Assess the morphology of the erythrocytes.
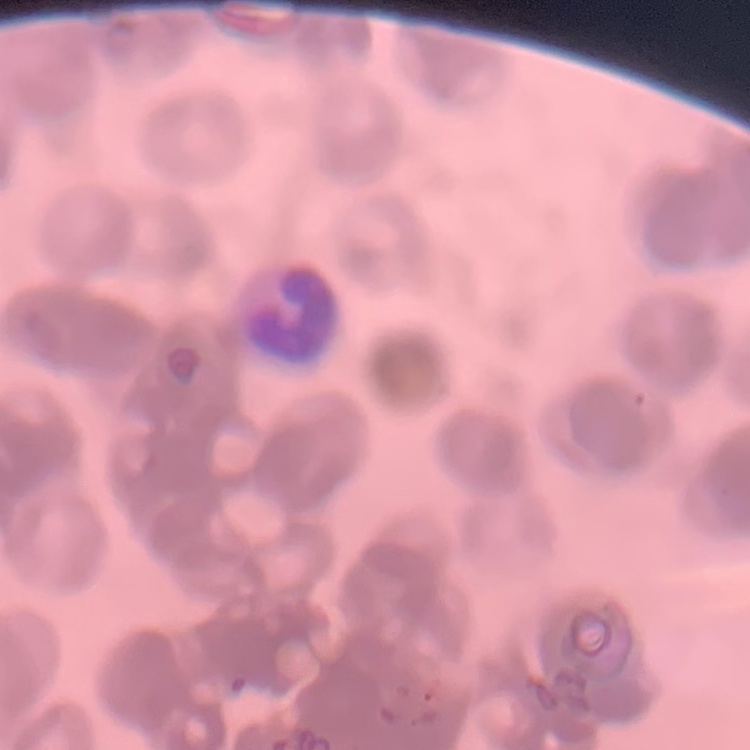

They show rouleaux formation.

Summary:
  - Stain: Field's or Giemsa
  - Image type: square crop of a larger photomicrograph
  - Preparation: thin peripheral smear